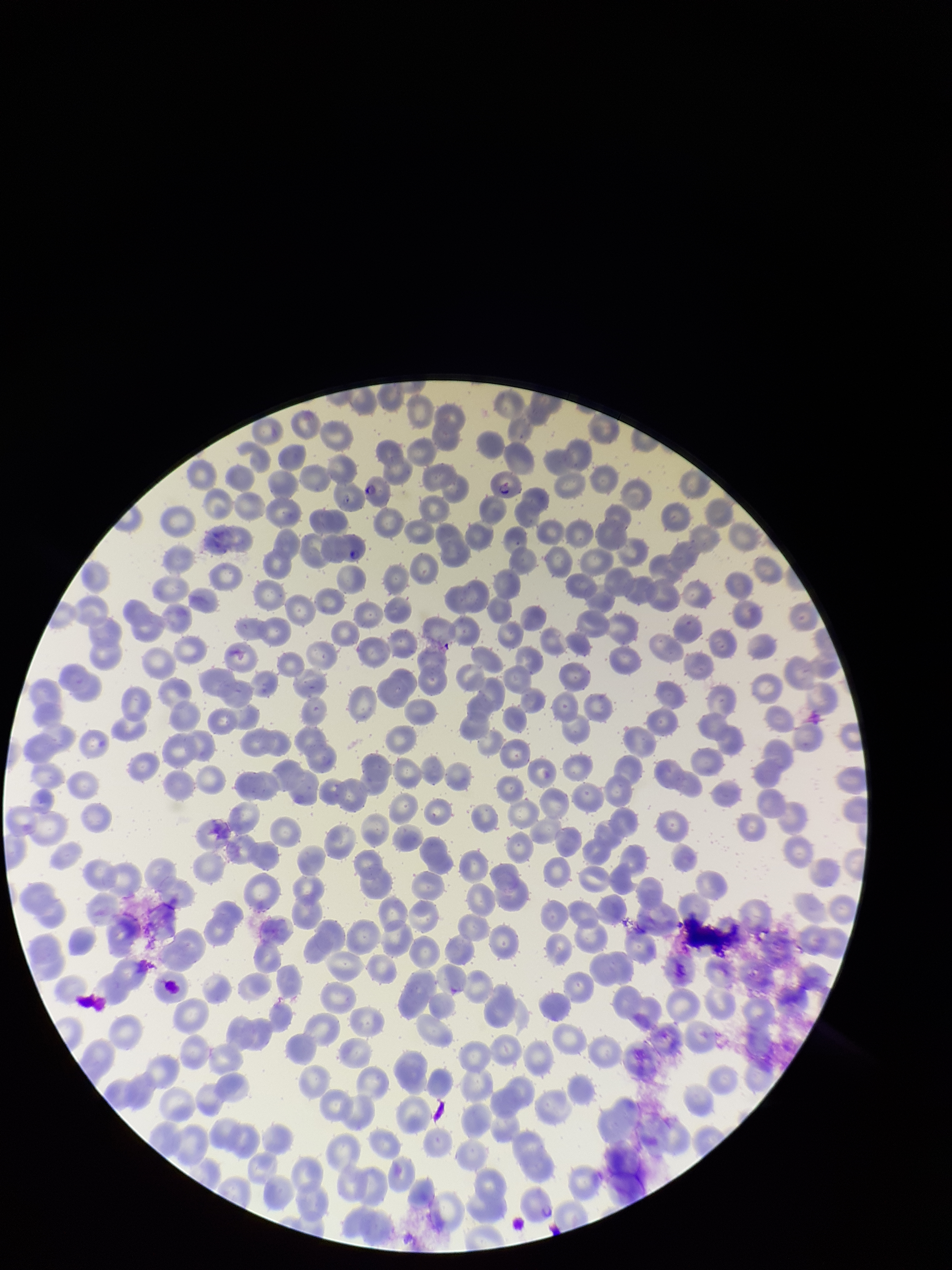

{
  "preparation": "thin",
  "field_of_view": "one from this slide",
  "species_reported_for_this_patient": "Plasmodium falciparum",
  "parasitized_red_blood_cells": "seen",
  "stain": "Giemsa",
  "image_size": "952×1270 pixels",
  "patient_malaria_status": "positive",
  "parasitized_red_blood_cell_count": 2,
  "red_blood_cell_count": 285,
  "capture": "smartphone photograph through the microscope eyepiece"
}